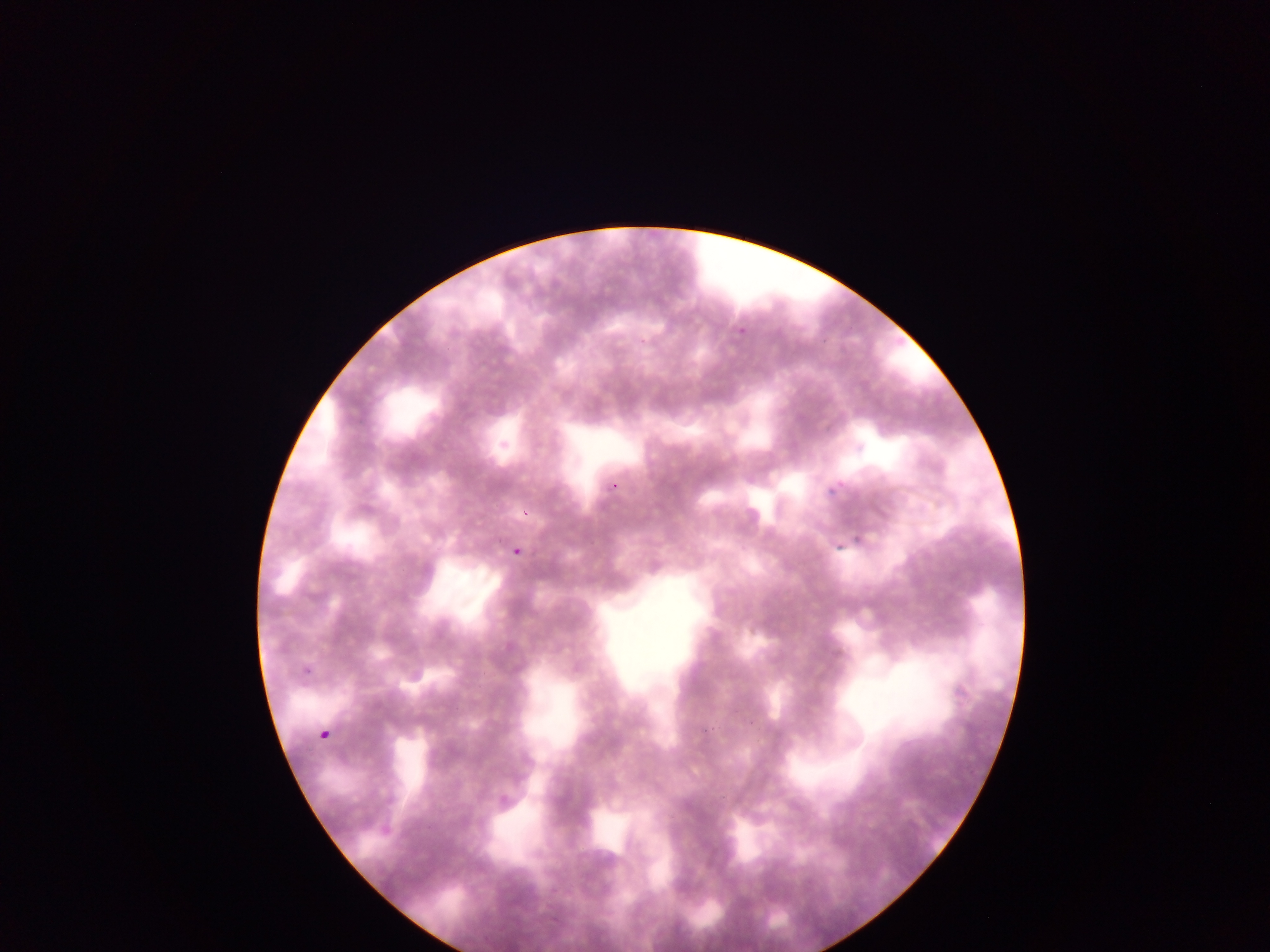

Approximate bounding boxes as left top right bottom in pixels.
Summary:
  - Malaria parasite locations: 734 324 748 337; 824 478 840 496; 850 528 868 551; 829 539 842 553; 508 544 531 558; 319 730 331 741
  - Image size: 1270×952 pixels
  - Field of view: single
  - Preparation: thin blood film
  - Country: Ghana
  - Capture: mobile-phone photograph through a microscope